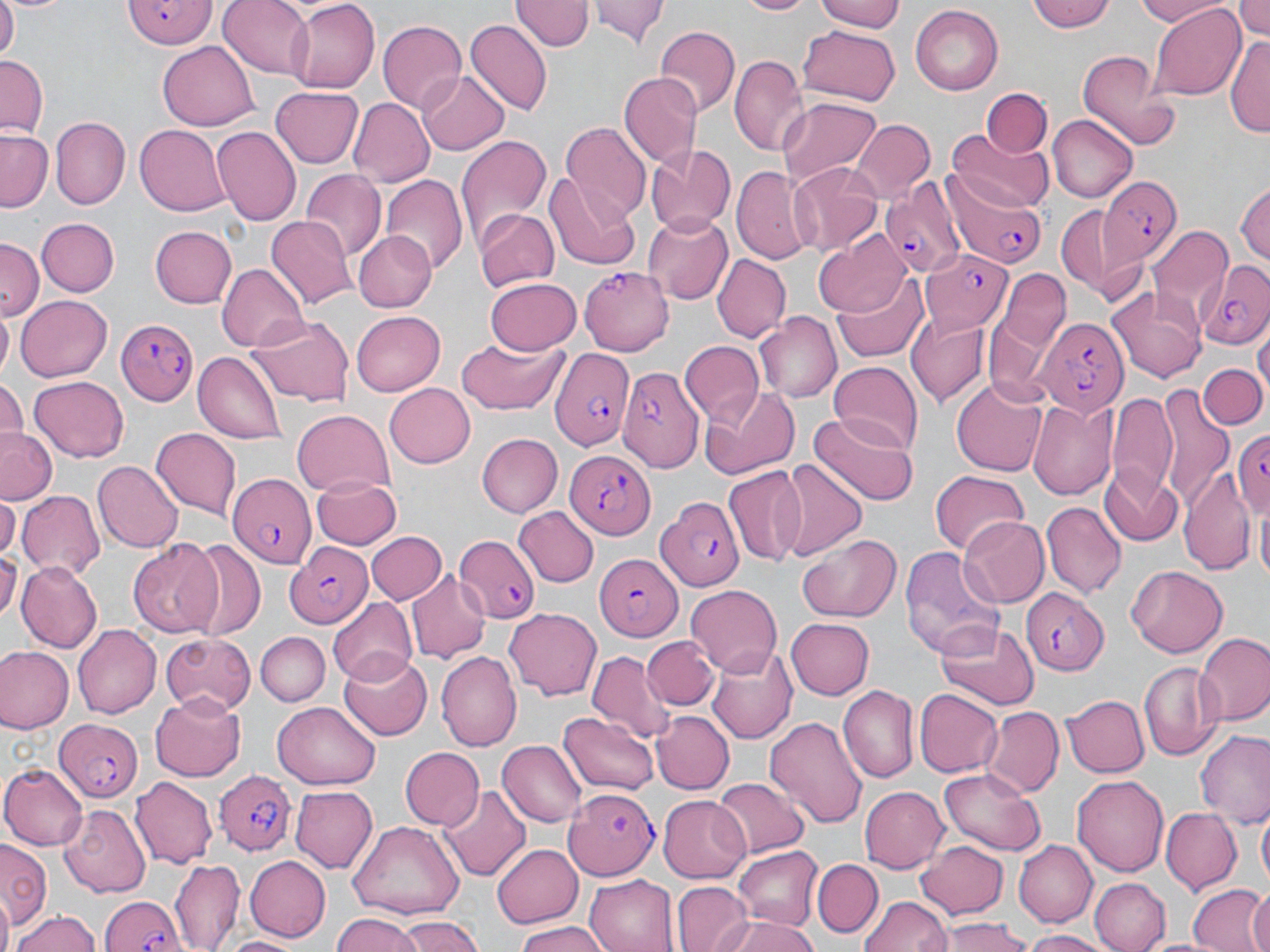

Summary:
  - Coordinate format: approximate bounding boxes as (x1,y1)-(x2,y2) corner pairs in pixels
  - Uninfected red blood cell locations: (0,0)-(20,56), (5,0)-(71,16), (219,0)-(318,79), (514,0)-(590,52), (591,0)-(669,47), (737,0)-(811,16), (813,0)-(908,33), (1028,0)-(1120,34), (1131,0)-(1228,25), (1232,0)-(1270,44), (282,1)-(380,93), (1149,3)-(1246,98), (909,6)-(1004,96), (377,18)-(467,113), (464,20)-(553,114), (797,24)-(900,106), (654,26)-(737,119), (1227,32)-(1270,141), (157,42)-(261,131), (1074,48)-(1178,150), (0,54)-(47,133), (731,54)-(808,158), (618,71)-(702,171), (416,72)-(510,155), (269,85)-(364,169), (981,89)-(1051,157), (346,97)-(434,187), (777,97)-(882,191), (1048,115)-(1137,202), (50,116)-(130,208), (854,119)-(935,199), (560,121)-(650,219), (135,124)-(230,217), (213,127)-(301,224), (948,129)-(1048,212), (0,130)-(51,214), (454,133)-(551,244), (645,141)-(736,233), (787,164)-(884,256), (733,166)-(809,266), (299,171)-(386,263), (380,173)-(467,274), (548,174)-(640,267), (1234,178)-(1270,275), (1054,202)-(1145,299), (473,208)-(557,294), (643,211)-(735,303), (266,215)-(356,312), (37,219)-(117,297), (1,221)-(96,318), (1149,223)-(1233,323), (150,225)-(237,308), (816,230)-(911,315), (353,232)-(435,313), (0,241)-(42,324), (713,254)-(790,342), (217,263)-(309,353), (835,270)-(929,360), (1000,270)-(1072,351), (484,277)-(581,356), (1106,286)-(1206,383), (16,293)-(113,381), (1,310)-(14,378), (756,311)-(841,404), (350,312)-(446,396), (905,312)-(989,406), (248,316)-(353,406), (1255,326)-(1269,400), (456,334)-(568,417), (679,339)-(763,425), (192,353)-(288,443), (827,360)-(924,453), (1198,361)-(1268,430), (30,374)-(131,461), (0,378)-(24,449), (951,380)-(1047,475), (385,383)-(476,467), (1152,383)-(1234,510), (701,384)-(797,478), (1102,393)-(1177,499), (1028,398)-(1117,500), (292,410)-(394,498), (809,411)-(921,506), (149,428)-(243,518), (1,430)-(61,503), (476,433)-(563,519), (773,456)-(867,560), (92,461)-(180,552), (1098,463)-(1184,544), (724,464)-(809,567), (1181,467)-(1253,578), (929,469)-(1032,556), (312,474)-(402,549), (17,491)-(105,577), (1,495)-(19,557), (1255,501)-(1270,588), (1043,502)-(1123,596), (516,506)-(599,588), (959,516)-(1049,609), (365,530)-(447,605), (798,533)-(901,623), (184,538)-(266,638), (127,541)-(225,638), (898,543)-(1003,664), (0,546)-(22,619), (17,562)-(102,654), (1125,565)-(1230,658), (408,571)-(490,661), (683,584)-(782,680), (328,597)-(417,684), (504,608)-(602,700), (786,618)-(875,698), (934,621)-(1040,712), (73,625)-(162,718), (255,631)-(331,706), (1197,633)-(1270,727), (159,635)-(256,714), (642,636)-(719,710), (709,646)-(797,745), (0,648)-(73,734), (584,648)-(674,741), (338,651)-(433,739), (437,652)-(523,749), (1140,661)-(1220,759), (837,686)-(919,783), (914,688)-(1004,778), (150,692)-(248,780), (1062,694)-(1149,778), (273,699)-(379,788), (981,706)-(1064,797), (560,710)-(657,791), (651,710)-(733,793), (766,716)-(866,832), (1197,728)-(1270,828), (499,739)-(588,828), (399,747)-(483,830), (0,763)-(87,848), (939,768)-(1046,856), (1072,775)-(1169,877), (129,778)-(217,869), (711,778)-(809,857), (859,785)-(948,871), (290,786)-(378,872), (439,786)-(530,883), (657,795)-(752,882), (58,806)-(149,897), (1159,807)-(1241,893), (1257,811)-(1270,886), (348,822)-(463,923), (918,840)-(1006,918), (1012,840)-(1095,928), (1,843)-(47,931), (491,843)-(582,930), (733,846)-(823,929), (247,855)-(332,940), (168,859)-(244,951), (812,859)-(884,938), (586,873)-(678,952), (1090,877)-(1170,952), (670,882)-(754,952), (1187,882)-(1269,952), (1243,886)-(1270,952), (859,895)-(954,952), (12,909)-(100,952), (717,913)-(818,952), (328,914)-(421,952), (392,917)-(487,952), (941,917)-(1031,952), (514,925)-(609,952), (1019,929)-(1104,952), (222,933)-(304,951)
  - Plasmodium falciparum-infected red blood cell locations: (118,2)-(217,49), (1103,176)-(1181,262), (881,181)-(965,279), (942,182)-(1050,265), (923,250)-(1013,330), (1199,262)-(1270,352), (580,266)-(675,355), (1037,317)-(1126,415), (116,320)-(195,406), (549,345)-(637,450), (615,360)-(701,472), (1228,426)-(1270,514), (564,449)-(657,540), (224,468)-(319,572), (656,500)-(745,590), (454,535)-(541,623), (282,543)-(371,628), (595,550)-(683,643), (1021,588)-(1109,673), (55,719)-(145,802), (215,769)-(296,859), (563,787)-(660,880), (100,894)-(188,952)
  - Slide-level diagnosis: Plasmodium falciparum
  - Image size: 1270×952 pixels
  - Modality: optical microscopy
  - Stain: May-Grünwald-Giemsa
  - Magnification: 1000x
  - Preparation: thin blood film
  - Field of view: one of a larger specimen